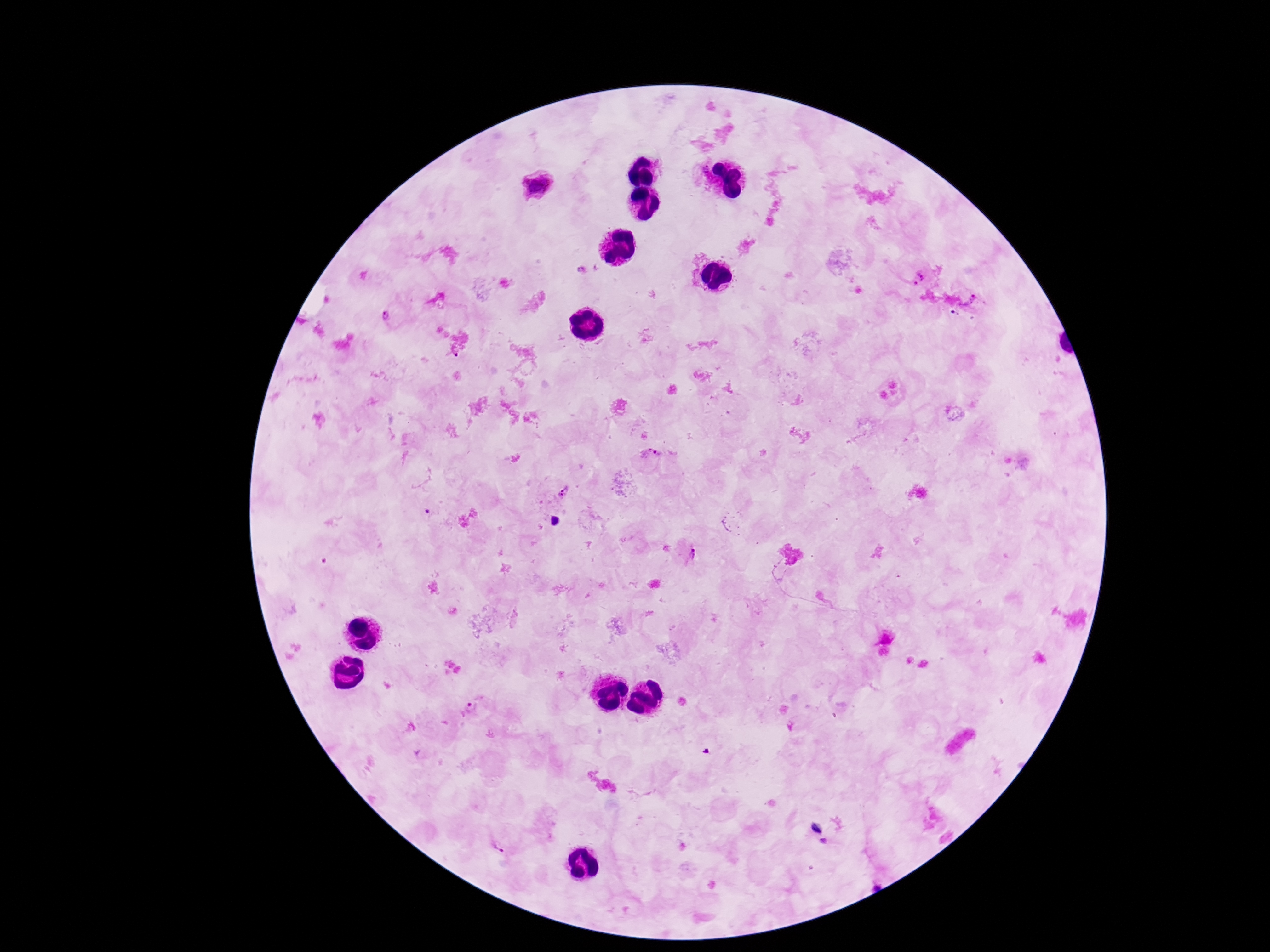

{
  "image_size": "1270×952 pixels",
  "patient_malaria_status": "infected",
  "plasmodium_parasite_locations": "approximate centers as [x, y] in pixels: [535, 186], [581, 269], [919, 276], [971, 300], [385, 314], [648, 456], [566, 491], [553, 520], [689, 553], [472, 708], [817, 830], [824, 840], [499, 846]",
  "capture": "smartphone camera through the microscope eyepiece",
  "preparation": "thick blood film",
  "stain": "Giemsa",
  "magnification": "100x",
  "field_of_view": "single"
}